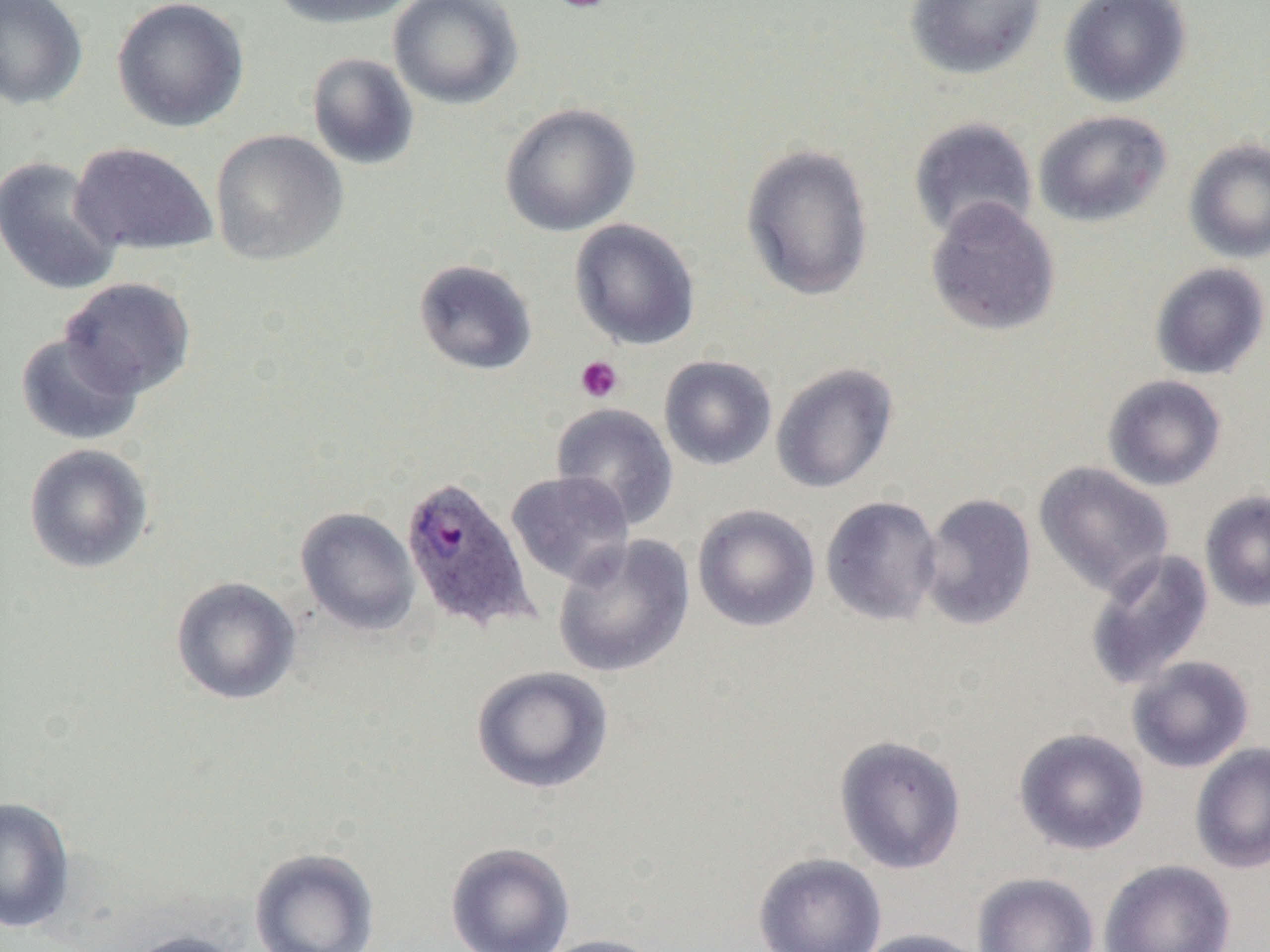
slide-level diagnosis = Plasmodium ovale
modality = light microscopy
magnification = 1000x
platelet locations = approximate bounding boxes as (x1,y1)-(x2,y2) corner pairs in pixels: (548,0)-(614,14), (575,355)-(623,403)
preparation = thin blood smear
field of view = single
Plasmodium ovale-infected red blood cell locations = approximate bounding boxes as (x1,y1)-(x2,y2) corner pairs in pixels: (400,474)-(537,633)
image size = 1270×952 pixels
uninfected red blood cell locations = approximate bounding boxes as (x1,y1)-(x2,y2) corner pairs in pixels: (0,0)-(88,110), (112,0)-(249,132), (268,0)-(419,29), (388,0)-(523,109), (904,0)-(1045,81), (1058,0)-(1192,108), (306,52)-(420,171), (499,103)-(641,237), (1033,110)-(1172,227), (908,116)-(1038,242), (210,129)-(349,266), (1184,138)-(1270,264), (70,142)-(218,256), (740,142)-(875,303), (0,155)-(123,296), (925,196)-(1060,337), (569,218)-(700,350), (413,259)-(538,376), (1149,262)-(1270,380), (60,277)-(196,399), (15,332)-(143,446), (659,355)-(777,470), (771,363)-(899,494), (1102,375)-(1226,491), (550,402)-(679,530), (24,443)-(154,574), (1033,462)-(1174,598), (506,470)-(635,587), (1200,490)-(1270,612), (918,492)-(1037,631), (820,496)-(942,626), (692,504)-(820,632), (295,507)-(420,636), (552,534)-(695,678), (1084,549)-(1215,690), (171,576)-(301,705), (1126,655)-(1254,774), (470,665)-(614,793), (1013,727)-(1150,856), (833,734)-(967,874), (1189,742)-(1270,874), (0,796)-(76,935), (445,841)-(576,952), (249,848)-(380,952), (753,851)-(887,952), (1098,859)-(1236,952), (972,872)-(1099,952), (853,928)-(992,952), (121,929)-(249,952), (535,933)-(668,952)